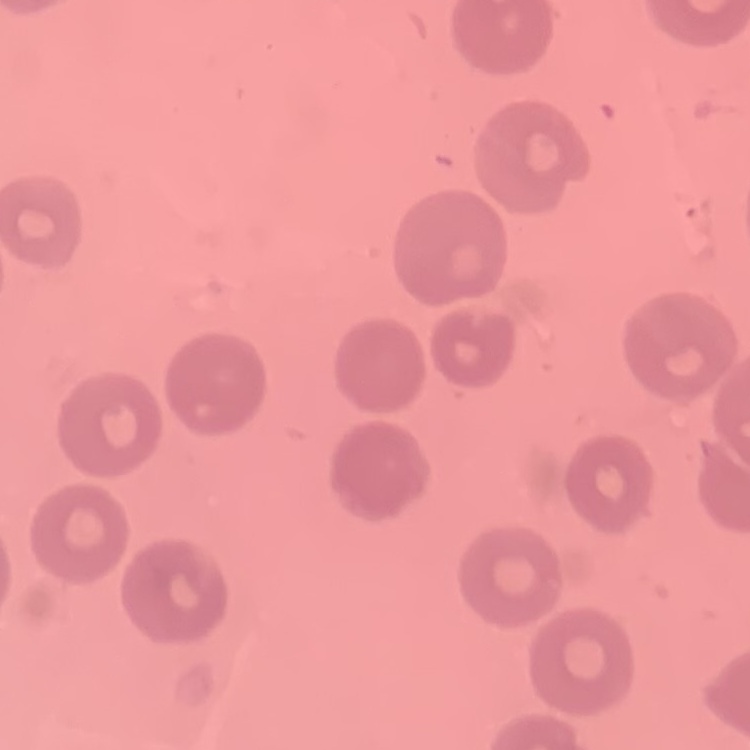
Summary:
  - Erythrocyte morphology: no rouleaux formation
  - Preparation: thin blood smear
  - Stain: Field's or Giemsa
  - Image type: square crop of a larger photomicrograph